Name the parasite shown.
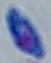
Toxoplasma gondii.

Summary:
  - Modality: photomicrograph
  - Magnification: 1000x